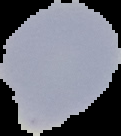

image type = segmented cell region on a black background
image size = 121×136 pixels
preparation = thin blood film
malaria status = uninfected